Classify this cell by malaria status.
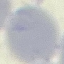

Uninfected.

Giemsa-stained preparation. Automatically extracted cell patch, resized to 64 × 64 pixels. Thin blood film. Acquired by smartphone through the microscope eyepiece.